Classify this cell by malaria status.
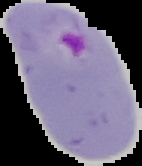
It is parasitized.

From a thin blood film. Cell region segmented out of the field of view; the surrounding area is masked to black. Image is 142×166 pixels.